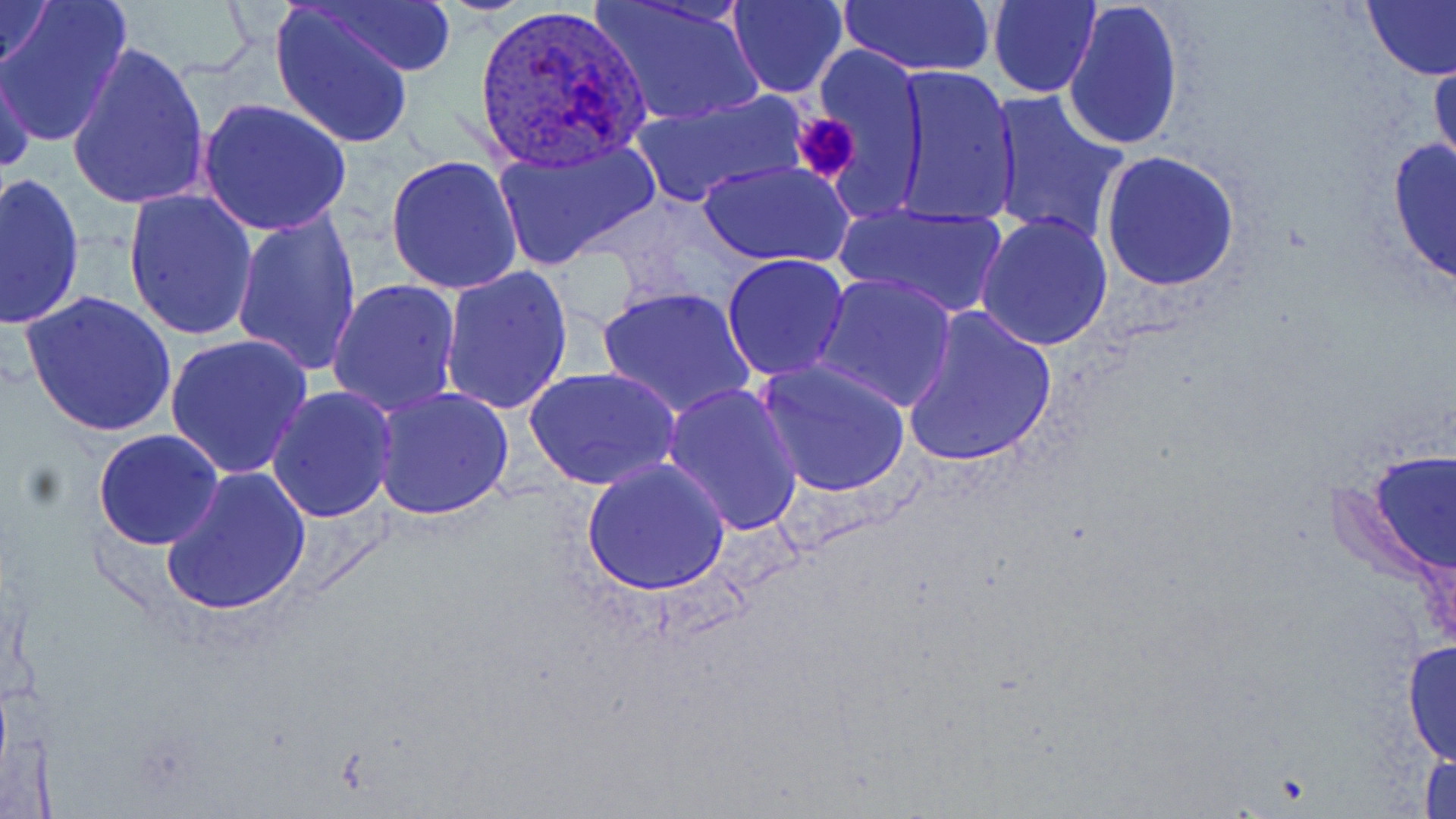
Summary:
  - Coordinate format: approximate bounding boxes as [x1, y1, x2, y2] in pixels
  - Platelet locations: [791, 112, 861, 183]
  - Plasmodium ovale-infected red blood cell locations: [474, 5, 652, 173]
  - Uninfected red blood cell locations: [0, 0, 133, 147], [0, 0, 56, 80], [314, 0, 457, 76], [592, 0, 761, 125], [727, 0, 848, 97], [839, 0, 996, 77], [1062, 0, 1184, 151], [989, 1, 1100, 97], [1361, 1, 1456, 82], [270, 2, 417, 150], [65, 41, 210, 211], [813, 44, 928, 196], [0, 54, 38, 179], [1429, 55, 1456, 178], [890, 65, 1021, 228], [984, 88, 1130, 245], [630, 90, 809, 208], [196, 97, 353, 238], [492, 138, 661, 268], [1385, 138, 1456, 289], [1098, 150, 1242, 292], [385, 155, 523, 295], [700, 161, 851, 268], [1, 175, 85, 329], [121, 191, 260, 343], [828, 201, 1012, 320], [231, 209, 364, 378], [975, 212, 1113, 351], [721, 254, 851, 382], [437, 266, 573, 417], [811, 272, 957, 413], [326, 278, 461, 418], [597, 285, 757, 421], [22, 291, 176, 438], [900, 307, 1059, 469], [165, 334, 314, 479], [756, 359, 910, 498], [524, 365, 681, 491], [662, 382, 803, 535], [266, 385, 399, 523], [372, 385, 516, 521], [91, 428, 224, 549], [1368, 451, 1456, 575], [581, 457, 730, 595], [159, 465, 311, 617], [1401, 637, 1456, 769], [1419, 750, 1456, 818]
  - Slide-level diagnosis: Plasmodium ovale
  - Modality: optical microscopy
  - Preparation: thin blood film
  - Image size: 1456×819 pixels
  - Field of view: one of a larger specimen
  - Stain: May-Grünwald-Giemsa
  - Magnification: 1000x